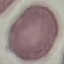

Summary:
  - Result: negative for malaria parasites
  - Stain: Giemsa
  - Capture: smartphone through the microscope eyepiece
  - Image type: automatically extracted cell patch, resized to 64 × 64 pixels
  - Preparation: thin smear